Assess this cell for malaria.
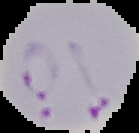
Parasitized.

Image is 139×133 pixels. From a thin blood film. The area outside the segmented cell region is set to black.